Classify this cell by malaria status.
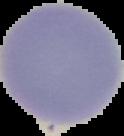

It is uninfected.

image type = cell region segmented out of the field of view; surrounding area masked to black
preparation = thin blood film
image size = 124×136 pixels